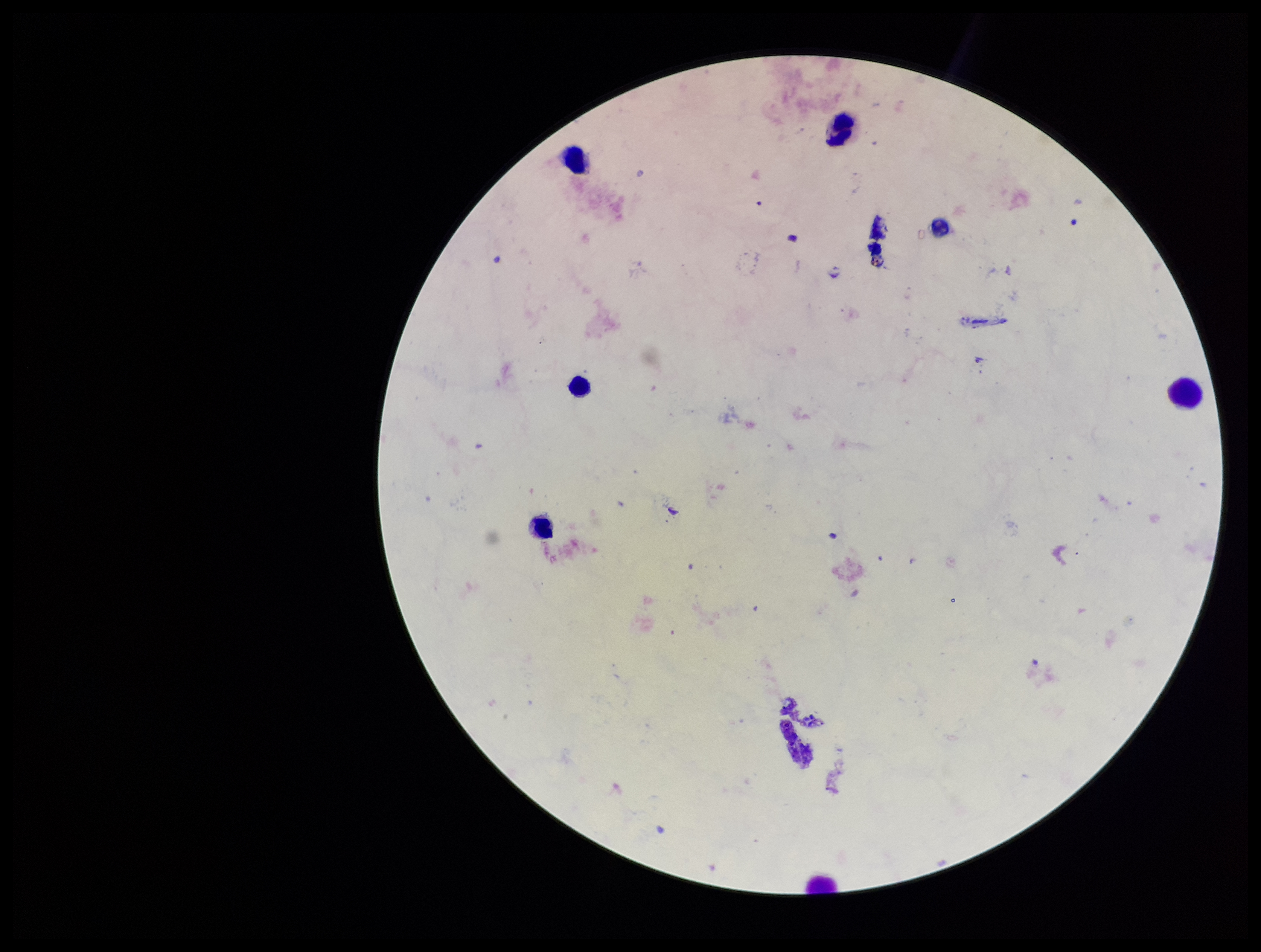

Leukocyte count: 7. Plasmodium parasites: none seen. Parasite count: 0. Stained with Giemsa. Image is 1261×952 pixels. Patient malaria status: negative. Photographed through the microscope eyepiece with a smartphone camera. Preparation: thick blood smear. One field from this slide.